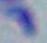
Summary:
  - Modality: micrograph
  - Identification: Toxoplasma gondii
  - Magnification: 1000x